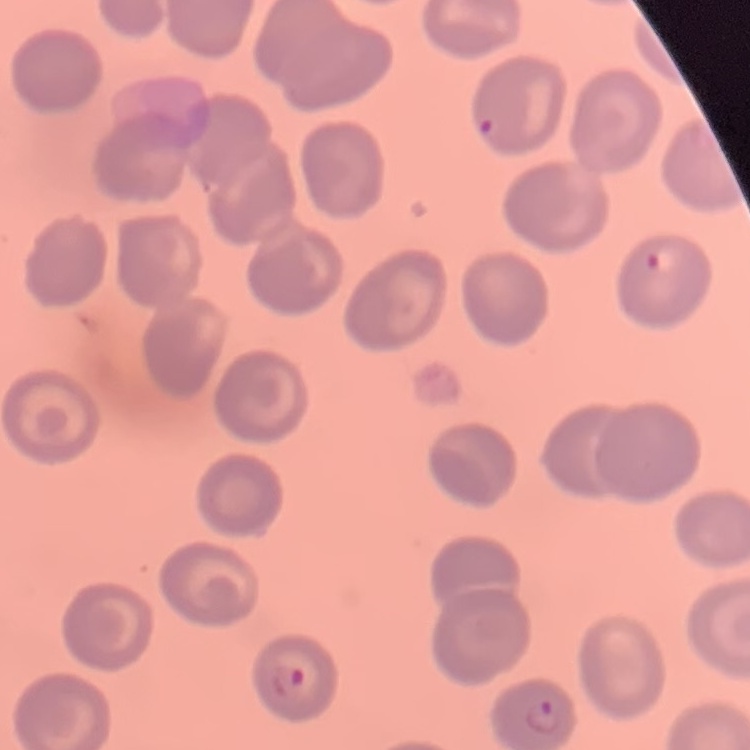

Summary:
  - Red blood cell morphology: no rouleaux formation
  - Stain: Field's or Giemsa
  - Preparation: thin blood smear
  - Image type: square crop of a larger photomicrograph